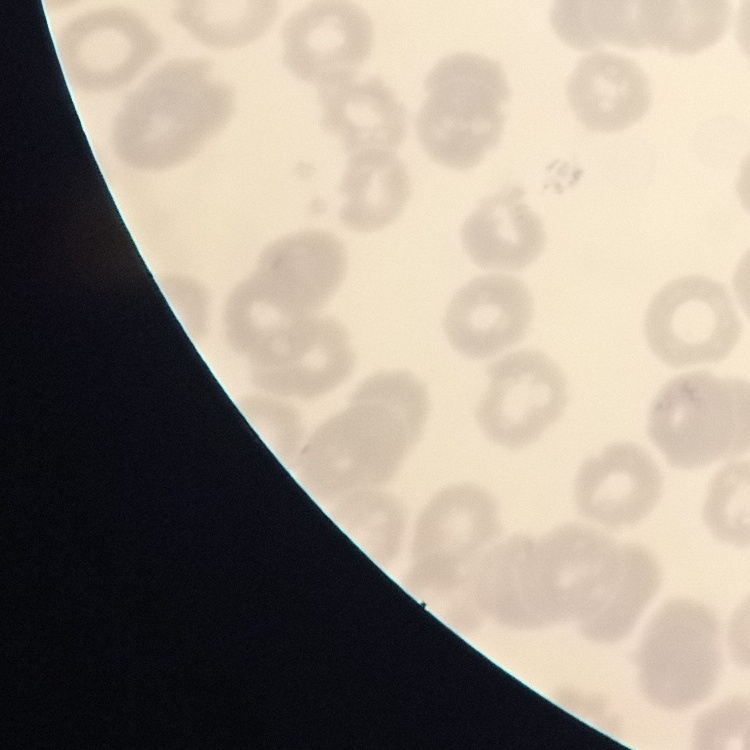
The red blood cells exhibit no rouleaux formation. Thin peripheral smear. Field's or Giemsa stain. Square crop of a larger photomicrograph.